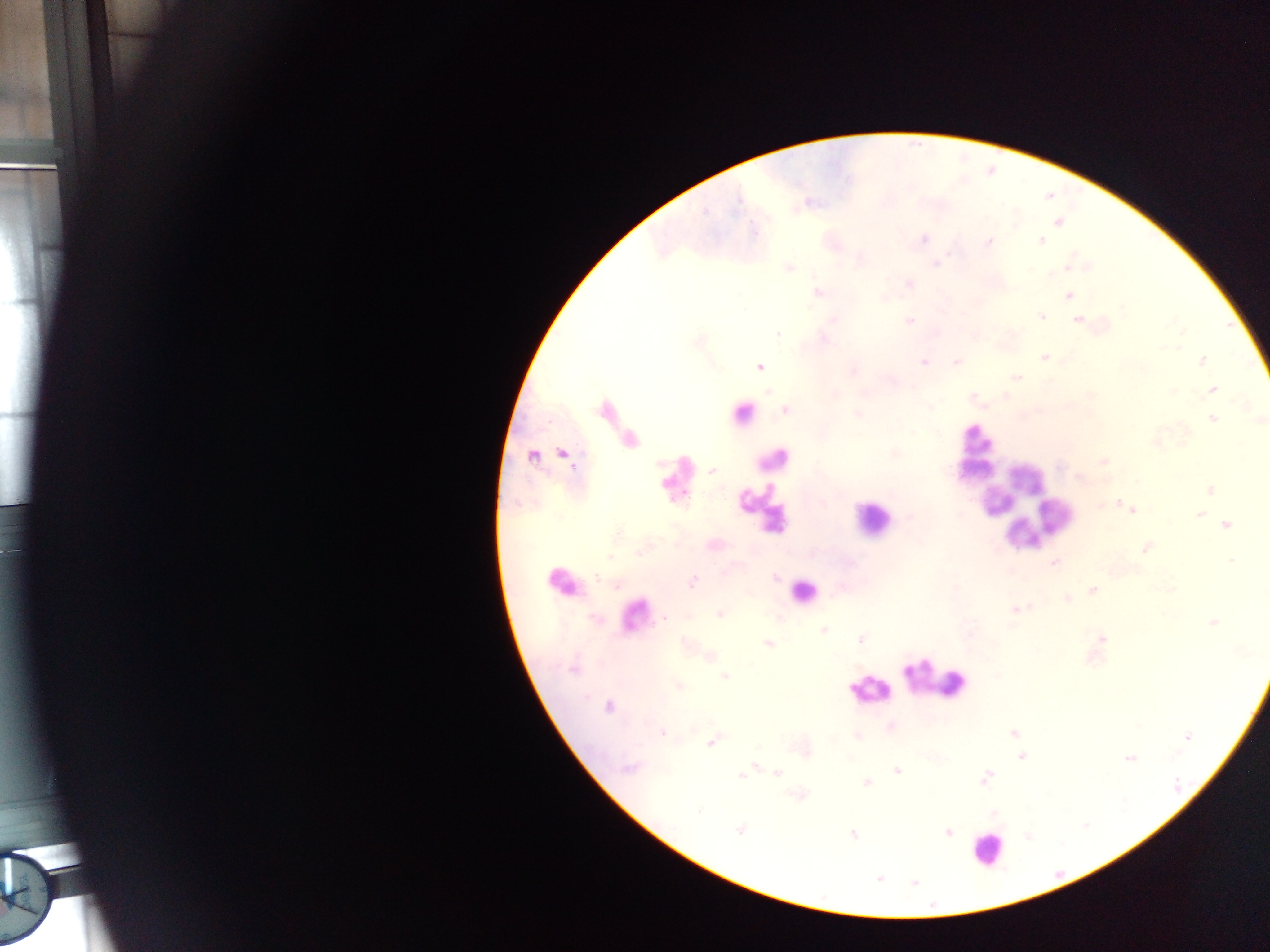

Approximate centers as x y in pixels.
Summary:
  - Leukocyte locations: 742 413; 974 447; 772 459; 676 479; 1025 505; 761 508; 1039 516; 872 519; 562 582; 803 591; 634 616; 937 679; 868 689; 987 849
  - Malaria parasite locations: 1058 222; 922 239; 988 242; 1041 242; 935 263; 1067 266; 788 267; 907 283; 818 292; 884 296; 1068 296; 1041 315; 1077 320; 909 321; 1045 358; 1202 360; 924 361; 956 361; 758 366; 1016 377; 1212 390; 1171 391; 604 409; 784 410; 858 414; 1212 418; 1258 420; 630 439; 562 454; 894 454; 532 456; 1103 460; 710 469; 1210 489; 1131 510; 1199 513; 1226 524; 1145 548; 1230 560; 1055 562; 773 577; 692 582; 1092 590; 1067 598; 1015 610; 718 614; 1212 621; 823 630; 1100 637; 861 639; 767 644; 708 656; 723 676; 677 686; 608 706; 890 726; 662 733; 1012 733; 856 736; 1186 736; 710 741; 806 752; 1022 756; 1128 758; 755 766; 629 767; 897 771; 740 772; 776 772; 983 778; 867 782; 993 813; 740 829; 947 831; 852 834; 878 878; 913 883
  - Country: Ghana
  - Field of view: single
  - Capture: mobile-phone photograph through a microscope
  - Preparation: thick blood smear
  - Image size: 1270×952 pixels